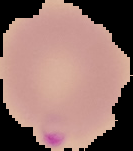

Summary:
  - Image type: cell region segmented out of the field of view; surrounding area masked to black
  - Image size: 133×151 pixels
  - Result: Plasmodium parasites identified
  - Preparation: thin blood film